Give the preparation type.
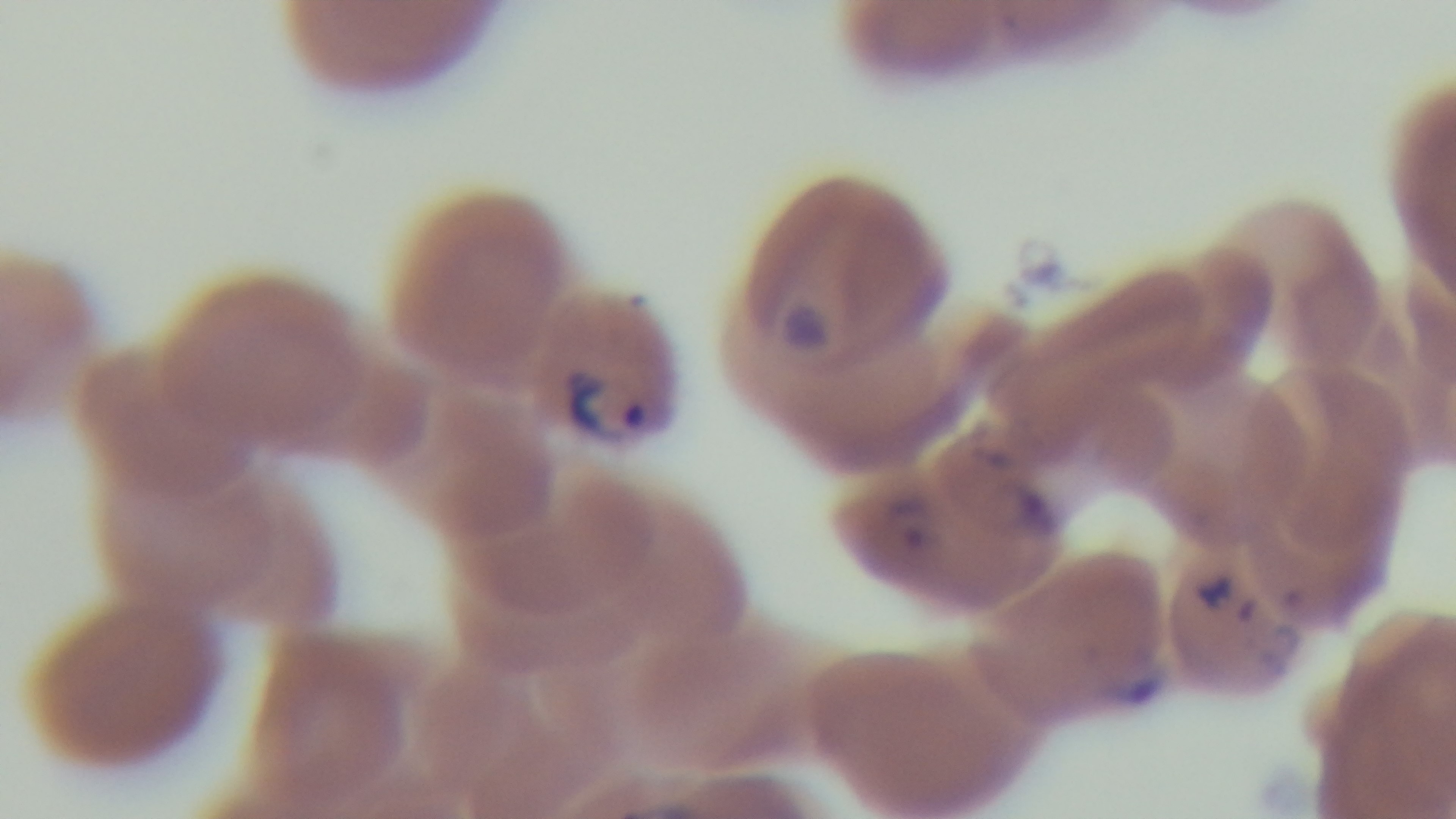

A thin smear.

objective: 100x oil immersion
modality: light microscopy
capture: mounted 4K digital camera
field_of_view: one from the slide
malaria_status: infected
stain: Giemsa